Assess for Plasmodium parasites.
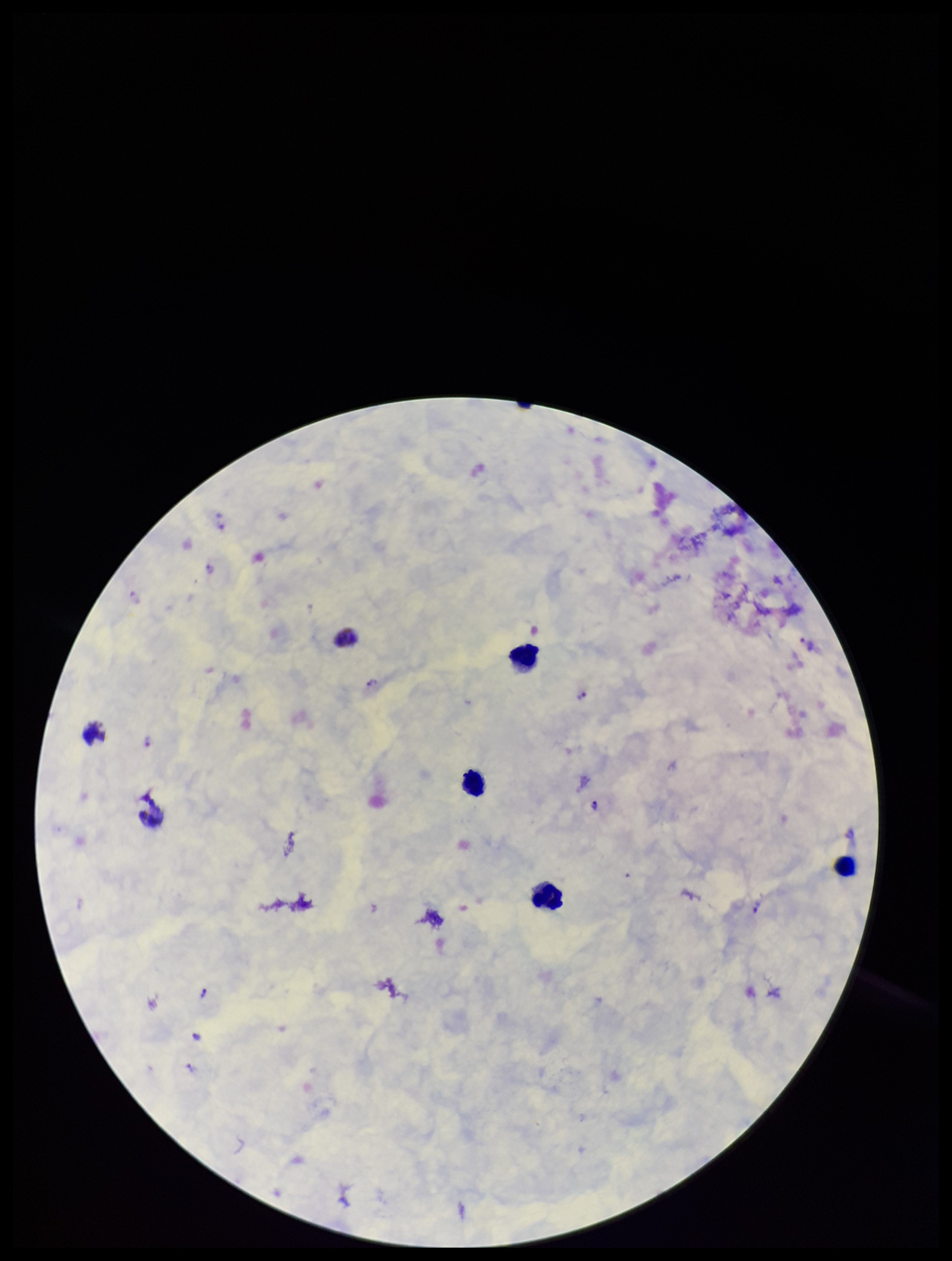
Detected.

Summary:
  - Leukocyte count: 6
  - Preparation: thick smear
  - Capture: smartphone photograph through the microscope eyepiece
  - Parasite count: 12
  - Species reported for this patient: Plasmodium vivax
  - Patient malaria status: infected
  - Stain: Giemsa
  - Field of view: single
  - Image size: 952×1261 pixels